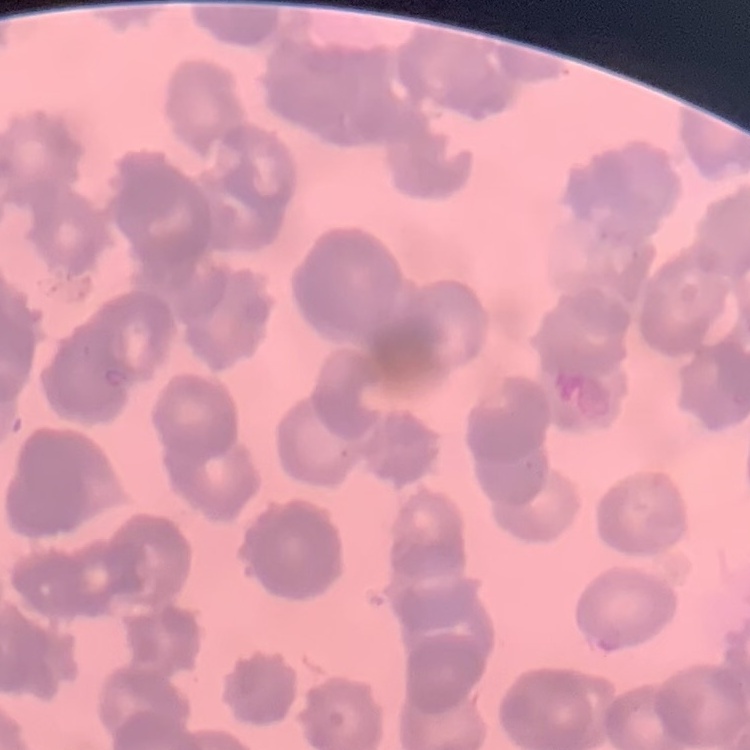
{
  "red_blood_cell_morphology": "rouleaux formation",
  "stain": "Field's or Giemsa",
  "preparation": "thin blood film",
  "image_type": "one tile cut from a larger photomicrograph"
}